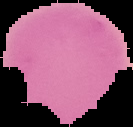
Image is 133×127 pixels. Segmented cell region on a black background. From a thin blood film. Malaria status: uninfected.